Classify this cell by malaria status.
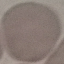
Uninfected.

Photographed with a smartphone camera at the microscope eyepiece. Automatically extracted cell patch, resized to 64 × 64 pixels. Giemsa-stained preparation. Thin blood film.